State which cell type is depicted.
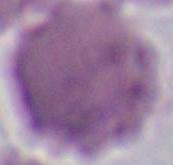
This is an erythrocyte.

{
  "modality": "photomicrograph",
  "magnification": "1000x"
}